Locate every P. falciparum parasite and give its life-cycle stage, and locate every leukocyte and any debris.
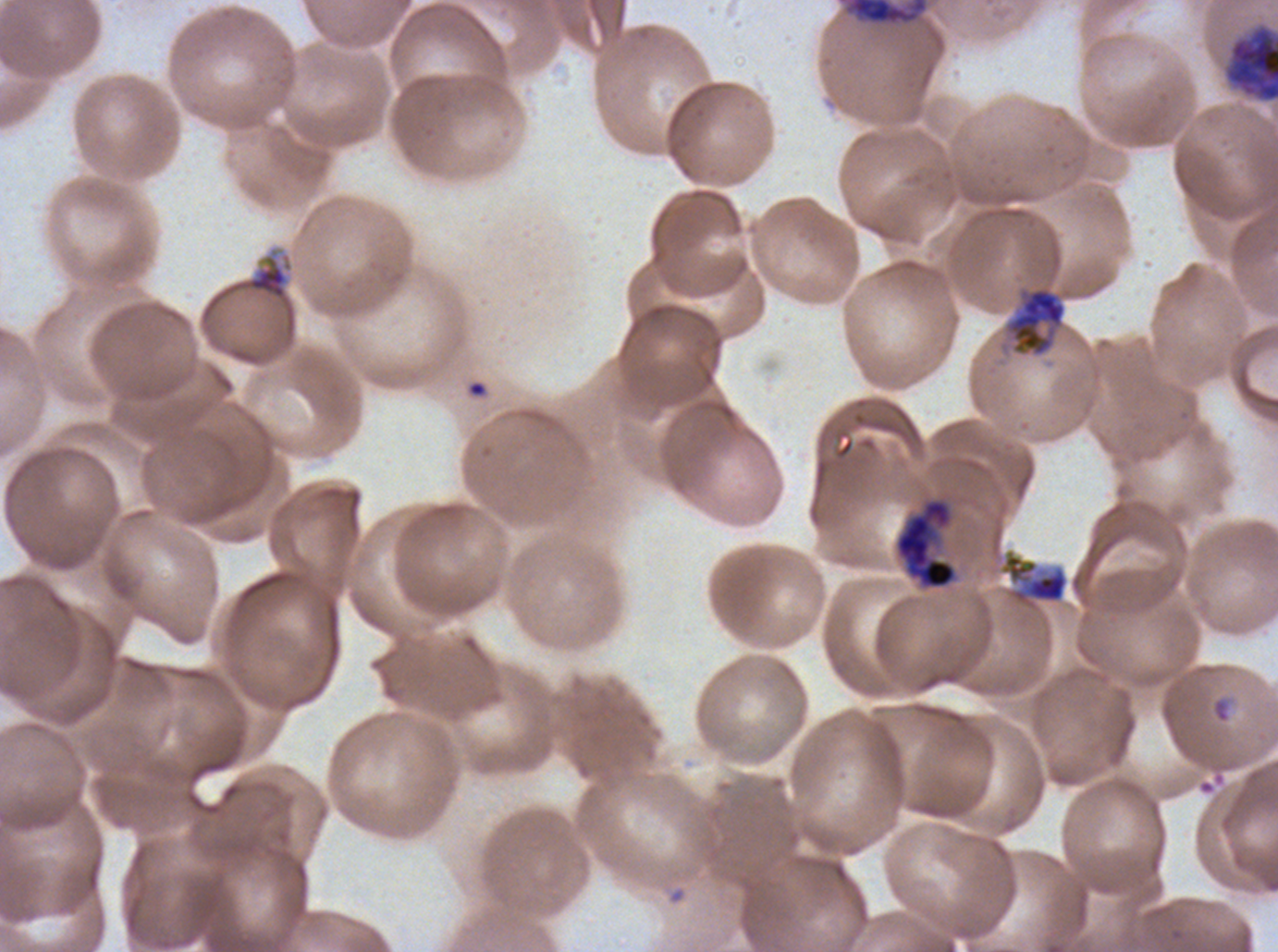
Approximate bounding boxes as {x1, y1, x2, y2} in pixels.
Rings: {1001, 553, 1068, 604}, {1211, 698, 1230, 723}.
Late trophozoites: {1004, 287, 1067, 357}.
Early schizonts: {1225, 26, 1277, 102}, {894, 497, 957, 590}.
Debris: {838, 0, 929, 27}, {247, 259, 288, 299}.
No late-ring/early-trophozoite forms, mid trophozoites, late schizonts, segmenters, gametocytes, or leukocytes observed.

Thin blood film. A sub-image separated from a larger composite. Giemsa stain. Life-cycle stages observed: ring, late trophozoite, early schizont. P. falciparum cultured ex vivo for 24 to 48 hours, from a patient in The Gambia. Image is 1278×952 pixels.